Identify the cell.
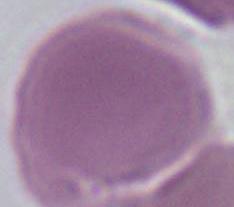

An erythrocyte.

modality = micrograph
magnification = 1000x